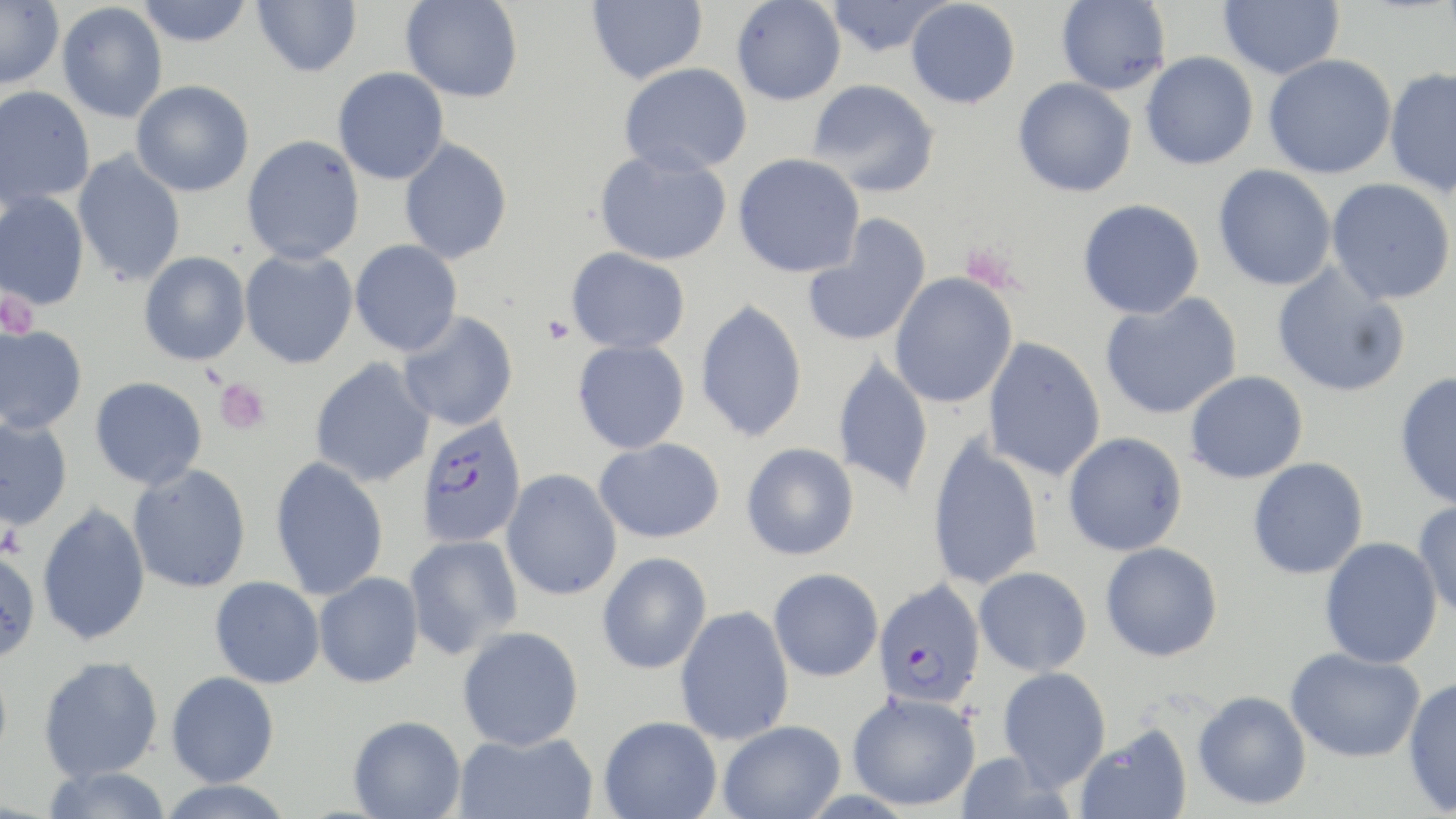

{
  "slide_level_diagnosis": "Plasmodium falciparum",
  "preparation": "thin blood film",
  "platelet_locations": "approximate bounding boxes as named x1/y1/x2/y2 corners in pixels: (x1=0, y1=291, x2=40, y2=337), (x1=542, y1=315, x2=575, y2=344), (x1=214, y1=377, x2=271, y2=435), (x1=0, y1=522, x2=26, y2=559)",
  "image_size": "1456×819 pixels",
  "modality": "light microscopy",
  "uninfected_red_blood_cell_locations": "approximate bounding boxes as named x1/y1/x2/y2 corners in pixels: (x1=252, y1=0, x2=362, y2=77), (x1=401, y1=0, x2=523, y2=102), (x1=587, y1=0, x2=707, y2=84), (x1=825, y1=0, x2=953, y2=57), (x1=906, y1=0, x2=1021, y2=109), (x1=1056, y1=0, x2=1171, y2=95), (x1=1219, y1=0, x2=1344, y2=80), (x1=0, y1=1, x2=64, y2=89), (x1=136, y1=1, x2=253, y2=46), (x1=731, y1=1, x2=846, y2=106), (x1=56, y1=2, x2=168, y2=123), (x1=1141, y1=51, x2=1258, y2=170), (x1=1263, y1=54, x2=1396, y2=179), (x1=619, y1=63, x2=753, y2=175), (x1=1384, y1=66, x2=1456, y2=198), (x1=333, y1=67, x2=449, y2=184), (x1=1013, y1=77, x2=1137, y2=197), (x1=807, y1=78, x2=940, y2=198), (x1=131, y1=80, x2=254, y2=197), (x1=0, y1=86, x2=95, y2=210), (x1=242, y1=134, x2=366, y2=264), (x1=399, y1=137, x2=513, y2=264), (x1=594, y1=147, x2=733, y2=266), (x1=73, y1=149, x2=187, y2=287), (x1=733, y1=153, x2=865, y2=278), (x1=1213, y1=164, x2=1337, y2=291), (x1=1326, y1=178, x2=1455, y2=305), (x1=0, y1=192, x2=90, y2=310), (x1=1077, y1=198, x2=1205, y2=319), (x1=802, y1=215, x2=932, y2=348), (x1=350, y1=240, x2=463, y2=356), (x1=566, y1=247, x2=691, y2=353), (x1=239, y1=248, x2=358, y2=369), (x1=139, y1=252, x2=251, y2=366), (x1=1272, y1=263, x2=1411, y2=398), (x1=888, y1=272, x2=1018, y2=409), (x1=1100, y1=292, x2=1243, y2=420), (x1=694, y1=298, x2=808, y2=443), (x1=397, y1=311, x2=519, y2=432), (x1=0, y1=324, x2=88, y2=434), (x1=982, y1=336, x2=1106, y2=481), (x1=572, y1=339, x2=690, y2=454), (x1=832, y1=354, x2=934, y2=499), (x1=310, y1=358, x2=436, y2=487), (x1=1185, y1=370, x2=1308, y2=484), (x1=1394, y1=372, x2=1456, y2=510), (x1=90, y1=376, x2=208, y2=489), (x1=0, y1=415, x2=73, y2=531), (x1=1063, y1=431, x2=1188, y2=556), (x1=927, y1=435, x2=1045, y2=590), (x1=594, y1=437, x2=725, y2=543), (x1=741, y1=442, x2=859, y2=560), (x1=270, y1=456, x2=389, y2=601), (x1=1247, y1=457, x2=1369, y2=580), (x1=128, y1=464, x2=252, y2=593), (x1=501, y1=469, x2=622, y2=600), (x1=1413, y1=499, x2=1456, y2=620), (x1=37, y1=501, x2=150, y2=646), (x1=403, y1=534, x2=524, y2=660), (x1=1319, y1=537, x2=1443, y2=669), (x1=1100, y1=541, x2=1223, y2=662), (x1=0, y1=550, x2=41, y2=662), (x1=597, y1=552, x2=713, y2=674), (x1=974, y1=566, x2=1092, y2=676), (x1=768, y1=567, x2=884, y2=681), (x1=314, y1=572, x2=424, y2=688), (x1=210, y1=576, x2=325, y2=688), (x1=674, y1=605, x2=795, y2=745), (x1=457, y1=626, x2=585, y2=751), (x1=1285, y1=646, x2=1425, y2=763), (x1=38, y1=655, x2=163, y2=782), (x1=997, y1=666, x2=1112, y2=790), (x1=166, y1=671, x2=279, y2=787), (x1=1402, y1=676, x2=1456, y2=815), (x1=846, y1=690, x2=982, y2=811), (x1=1193, y1=690, x2=1311, y2=810), (x1=348, y1=715, x2=466, y2=819), (x1=598, y1=715, x2=722, y2=819), (x1=718, y1=720, x2=846, y2=819), (x1=1075, y1=723, x2=1193, y2=819), (x1=454, y1=730, x2=598, y2=819), (x1=953, y1=753, x2=1071, y2=819), (x1=40, y1=766, x2=173, y2=819), (x1=154, y1=779, x2=297, y2=818)",
  "stain": "May-Grünwald-Giemsa",
  "magnification": "1000x",
  "plasmodium_falciparum_infected_red_blood_cell_locations": "approximate bounding boxes as named x1/y1/x2/y2 corners in pixels: (x1=415, y1=413, x2=528, y2=549), (x1=872, y1=579, x2=987, y2=709)",
  "field_of_view": "single"
}